Rate the background quality.
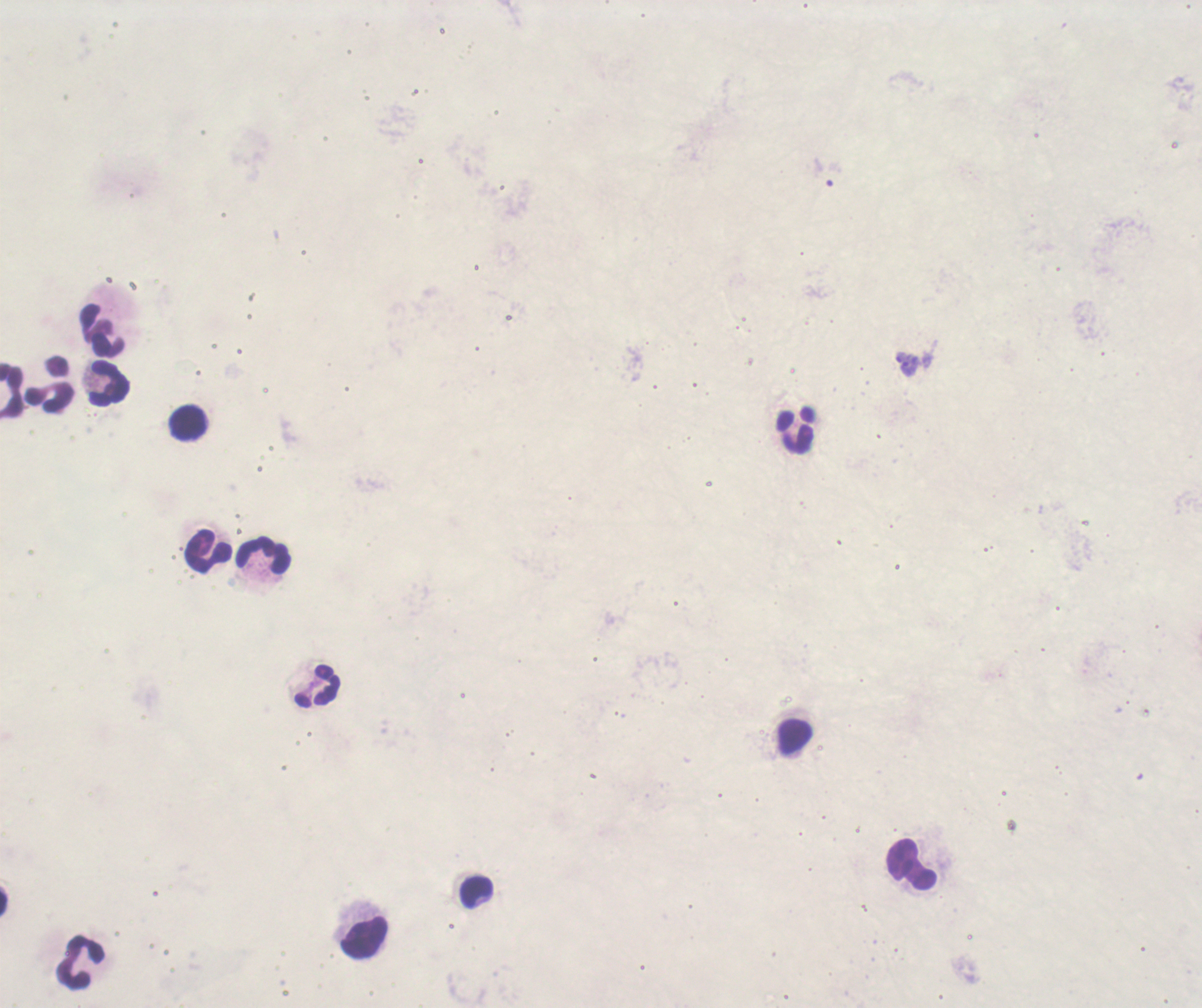

Poor.

Approximate centers as (x, y) in pixels. Leukocyte locations: (103, 329), (107, 381), (13, 385), (52, 385), (189, 423), (795, 429), (204, 550), (263, 556), (315, 686), (793, 738), (912, 863), (474, 893), (365, 940), (81, 961). 100x magnification. Previously used in a real diagnosis. One field from this slide. Coloration quality: bad. Result: no malaria parasites detected. Romanowsky stain. Thick blood film. Image is 1202×1008 pixels.